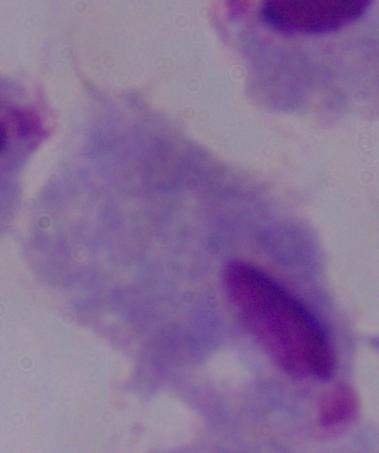 Photomicrograph. A trichomonad is seen. 1000x magnification.